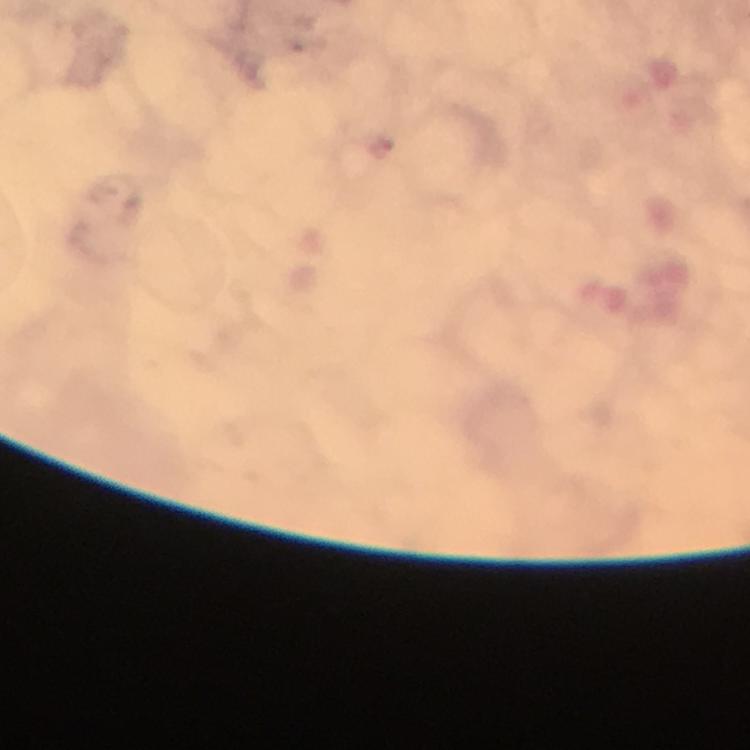

Approximate centers as [x, y] in pixels. Plasmodium parasite locations: [380, 147]. Image is 750×750 pixels. Giemsa-stained preparation. A crop from one field of view. 100x magnification. Immersion oil applied. From a malaria diagnostic workup. Photographed through the microscope with a smartphone camera. Thick blood film.